Name the blood parasite species.
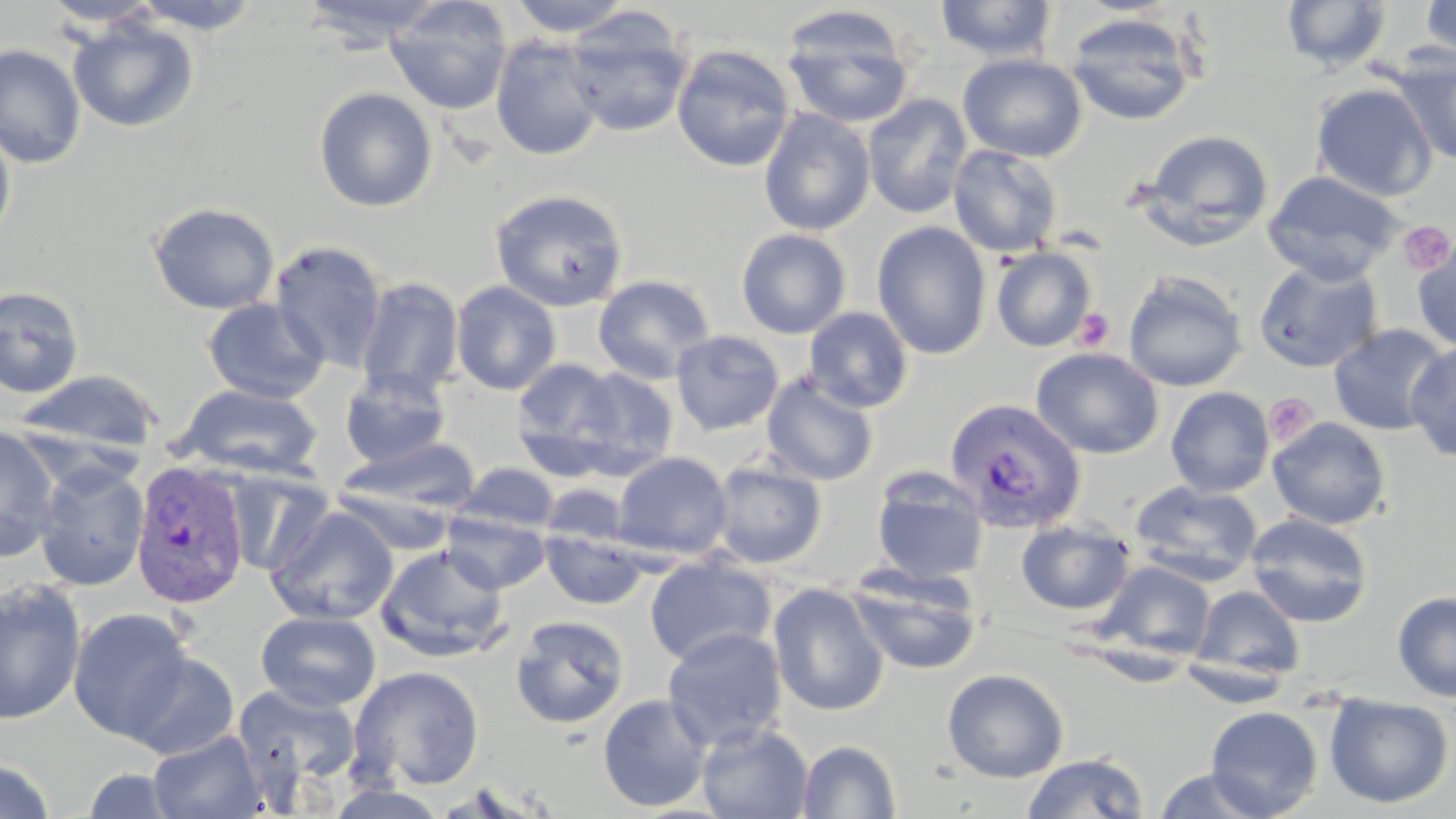
Plasmodium vivax.

Summary:
  - Coordinate format: approximate bounding boxes as named x1/y1/x2/y2 corners in pixels
  - Uninfected red blood cell locations: (x1=128, y1=0, x2=265, y2=34), (x1=296, y1=0, x2=448, y2=50), (x1=385, y1=0, x2=513, y2=115), (x1=507, y1=0, x2=637, y2=38), (x1=935, y1=0, x2=1058, y2=62), (x1=1419, y1=0, x2=1455, y2=62), (x1=42, y1=1, x2=164, y2=30), (x1=1282, y1=1, x2=1392, y2=74), (x1=780, y1=6, x2=916, y2=129), (x1=562, y1=8, x2=694, y2=138), (x1=1064, y1=12, x2=1201, y2=126), (x1=67, y1=17, x2=200, y2=133), (x1=489, y1=35, x2=605, y2=161), (x1=0, y1=43, x2=86, y2=169), (x1=672, y1=44, x2=796, y2=172), (x1=1389, y1=50, x2=1455, y2=165), (x1=957, y1=53, x2=1086, y2=163), (x1=1310, y1=82, x2=1438, y2=202), (x1=314, y1=86, x2=438, y2=212), (x1=862, y1=93, x2=973, y2=219), (x1=758, y1=107, x2=875, y2=236), (x1=0, y1=121, x2=16, y2=250), (x1=1139, y1=129, x2=1274, y2=247), (x1=947, y1=144, x2=1064, y2=258), (x1=1262, y1=169, x2=1403, y2=284), (x1=489, y1=189, x2=629, y2=312), (x1=147, y1=202, x2=281, y2=315), (x1=872, y1=221, x2=992, y2=359), (x1=736, y1=228, x2=851, y2=339), (x1=1412, y1=235, x2=1456, y2=352), (x1=269, y1=240, x2=388, y2=373), (x1=991, y1=247, x2=1097, y2=351), (x1=1253, y1=258, x2=1383, y2=374), (x1=1123, y1=270, x2=1249, y2=393), (x1=593, y1=275, x2=716, y2=385), (x1=355, y1=277, x2=464, y2=402), (x1=451, y1=280, x2=561, y2=395), (x1=0, y1=285, x2=85, y2=399), (x1=202, y1=298, x2=329, y2=404), (x1=804, y1=307, x2=914, y2=413), (x1=1327, y1=323, x2=1452, y2=435), (x1=670, y1=330, x2=784, y2=436), (x1=1405, y1=342, x2=1456, y2=463), (x1=1031, y1=346, x2=1163, y2=460), (x1=511, y1=359, x2=630, y2=479), (x1=561, y1=365, x2=680, y2=479), (x1=14, y1=368, x2=164, y2=454), (x1=339, y1=368, x2=451, y2=470), (x1=762, y1=371, x2=880, y2=487), (x1=178, y1=384, x2=323, y2=480), (x1=1165, y1=386, x2=1275, y2=498), (x1=1267, y1=417, x2=1391, y2=530), (x1=0, y1=426, x2=61, y2=560), (x1=337, y1=437, x2=482, y2=518), (x1=612, y1=451, x2=732, y2=560), (x1=709, y1=459, x2=828, y2=569), (x1=33, y1=461, x2=150, y2=591), (x1=457, y1=462, x2=558, y2=536), (x1=224, y1=468, x2=335, y2=577), (x1=870, y1=468, x2=989, y2=584), (x1=1129, y1=480, x2=1262, y2=586), (x1=540, y1=483, x2=631, y2=548), (x1=266, y1=506, x2=399, y2=626), (x1=441, y1=508, x2=550, y2=594), (x1=1245, y1=512, x2=1374, y2=628), (x1=1015, y1=519, x2=1135, y2=616), (x1=541, y1=527, x2=650, y2=611), (x1=375, y1=545, x2=510, y2=663), (x1=644, y1=555, x2=776, y2=667), (x1=1096, y1=560, x2=1215, y2=662), (x1=846, y1=562, x2=984, y2=676), (x1=0, y1=579, x2=85, y2=725), (x1=768, y1=582, x2=891, y2=716), (x1=1191, y1=584, x2=1306, y2=682), (x1=1392, y1=590, x2=1456, y2=702), (x1=67, y1=607, x2=194, y2=742), (x1=255, y1=610, x2=381, y2=712), (x1=510, y1=614, x2=630, y2=729), (x1=662, y1=626, x2=788, y2=751), (x1=123, y1=651, x2=240, y2=760), (x1=349, y1=665, x2=486, y2=791), (x1=941, y1=668, x2=1069, y2=783), (x1=233, y1=684, x2=362, y2=802), (x1=597, y1=693, x2=713, y2=813), (x1=1324, y1=694, x2=1454, y2=809), (x1=1205, y1=705, x2=1323, y2=817), (x1=696, y1=722, x2=813, y2=819), (x1=147, y1=729, x2=268, y2=818), (x1=797, y1=739, x2=902, y2=818), (x1=1021, y1=752, x2=1150, y2=818), (x1=0, y1=758, x2=57, y2=819), (x1=78, y1=766, x2=184, y2=818), (x1=1150, y1=767, x2=1277, y2=818)
  - Platelet locations: (x1=1398, y1=220, x2=1454, y2=275), (x1=1074, y1=308, x2=1115, y2=350), (x1=1265, y1=392, x2=1319, y2=447)
  - Plasmodium vivax-infected red blood cell locations: (x1=944, y1=396, x2=1088, y2=533), (x1=130, y1=459, x2=251, y2=609)
  - Preparation: thin blood smear
  - Field of view: one of a larger specimen
  - Magnification: 1000x
  - Modality: optical microscopy
  - Image size: 1456×819 pixels
  - Stain: May-Grünwald-Giemsa